Locate and identify every blood parasite.
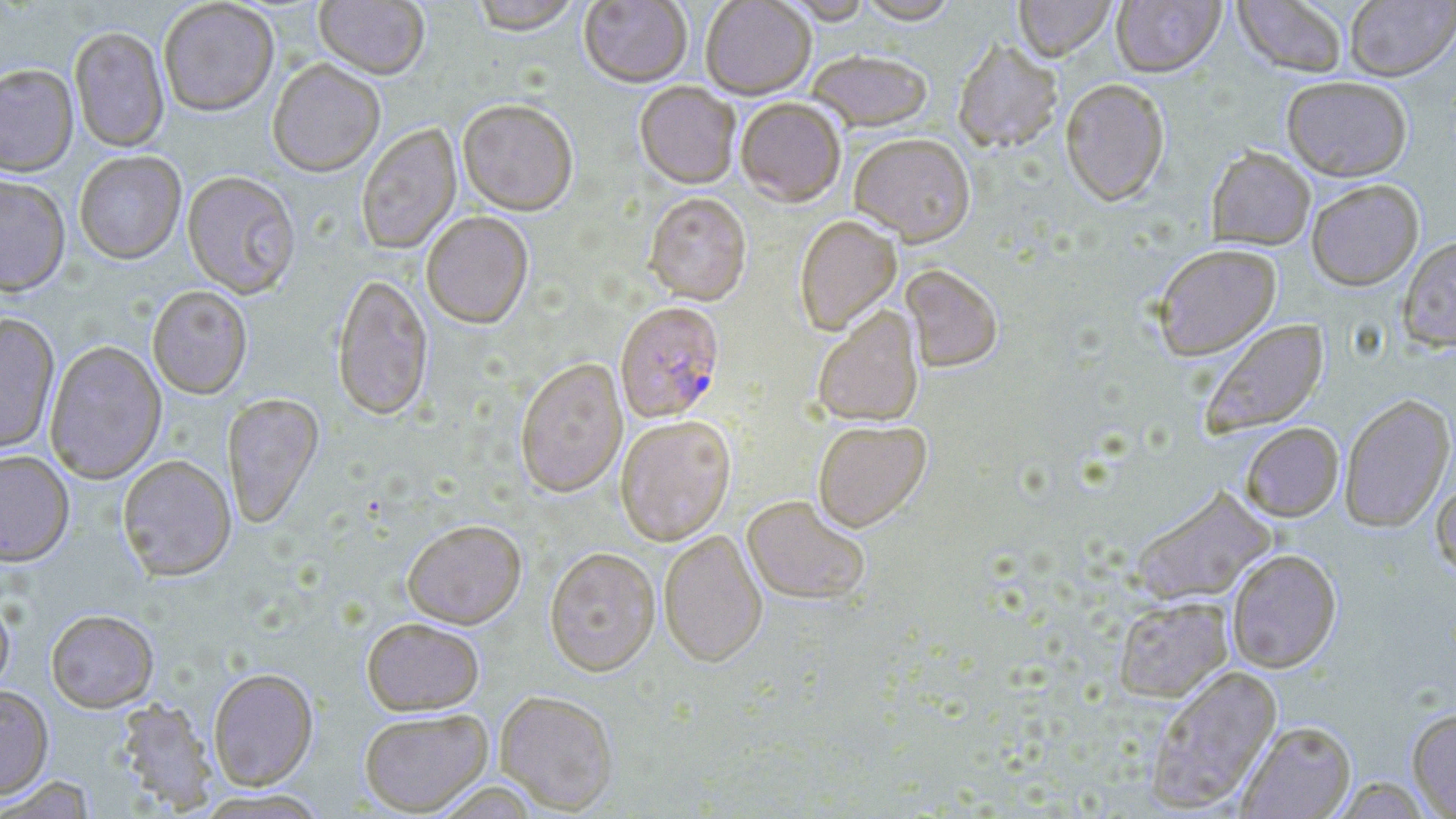
Approximate bounding boxes as (x1, y1, x2, y2) in pixels.
Plasmodium falciparum-infected red blood cells: (615, 304, 726, 425).
No Plasmodium ovale, Plasmodium malariae, Plasmodium vivax, Babesia divergens, or Trypanosoma brucei observed.

Uninfected red blood cell locations: (314, 0, 429, 83), (470, 0, 582, 39), (579, 0, 692, 90), (701, 0, 816, 102), (776, 0, 873, 27), (858, 0, 959, 28), (1014, 0, 1116, 64), (1112, 0, 1225, 78), (1233, 0, 1349, 77), (1345, 0, 1456, 81), (158, 1, 279, 120), (69, 28, 170, 154), (953, 43, 1063, 156), (808, 53, 932, 134), (267, 62, 385, 180), (0, 67, 79, 180), (1282, 75, 1412, 181), (1060, 79, 1170, 207), (634, 83, 740, 192), (736, 100, 846, 210), (457, 102, 578, 219), (356, 124, 463, 257), (849, 136, 975, 250), (1206, 147, 1315, 250), (74, 153, 187, 267), (182, 173, 300, 302), (0, 178, 71, 300), (1306, 179, 1423, 289), (643, 195, 752, 308), (422, 215, 534, 331), (794, 217, 902, 337), (1398, 234, 1456, 352), (1153, 244, 1281, 360), (901, 267, 1003, 375), (332, 277, 433, 423), (147, 288, 253, 401), (813, 308, 924, 429), (0, 316, 60, 456), (1198, 318, 1329, 438), (45, 342, 167, 485), (515, 360, 628, 500), (1339, 393, 1455, 532), (223, 394, 325, 530), (616, 418, 736, 548), (813, 422, 932, 535), (1240, 423, 1343, 521), (0, 453, 74, 570), (117, 457, 237, 584), (1432, 476, 1456, 580), (1131, 484, 1277, 606), (740, 497, 870, 607), (403, 523, 527, 632), (659, 531, 768, 670), (1227, 549, 1342, 673), (545, 550, 660, 680), (1113, 596, 1234, 703), (0, 597, 15, 701), (46, 612, 159, 714), (361, 621, 484, 717), (1145, 665, 1282, 811), (209, 671, 319, 792), (0, 686, 54, 801), (495, 693, 618, 815), (114, 700, 219, 815), (1407, 706, 1456, 818), (359, 712, 494, 817), (1237, 720, 1356, 818), (1, 777, 97, 818), (432, 782, 542, 819), (193, 789, 331, 818). Slide-level diagnosis: Plasmodium falciparum. Image is 1456×819 pixels. May-Grünwald-Giemsa-stained preparation. Single field of view. Thin blood smear. Captured at 1000x magnification. Light microscopy.